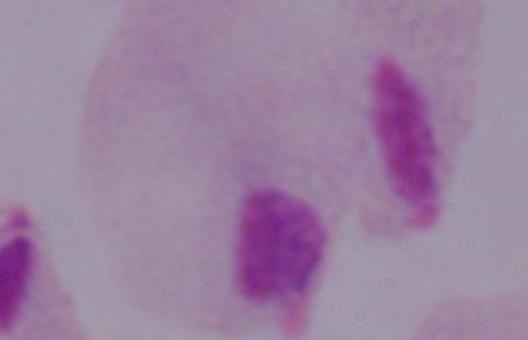

Captured at 1000x magnification. A trichomonad is shown. Photomicrograph.